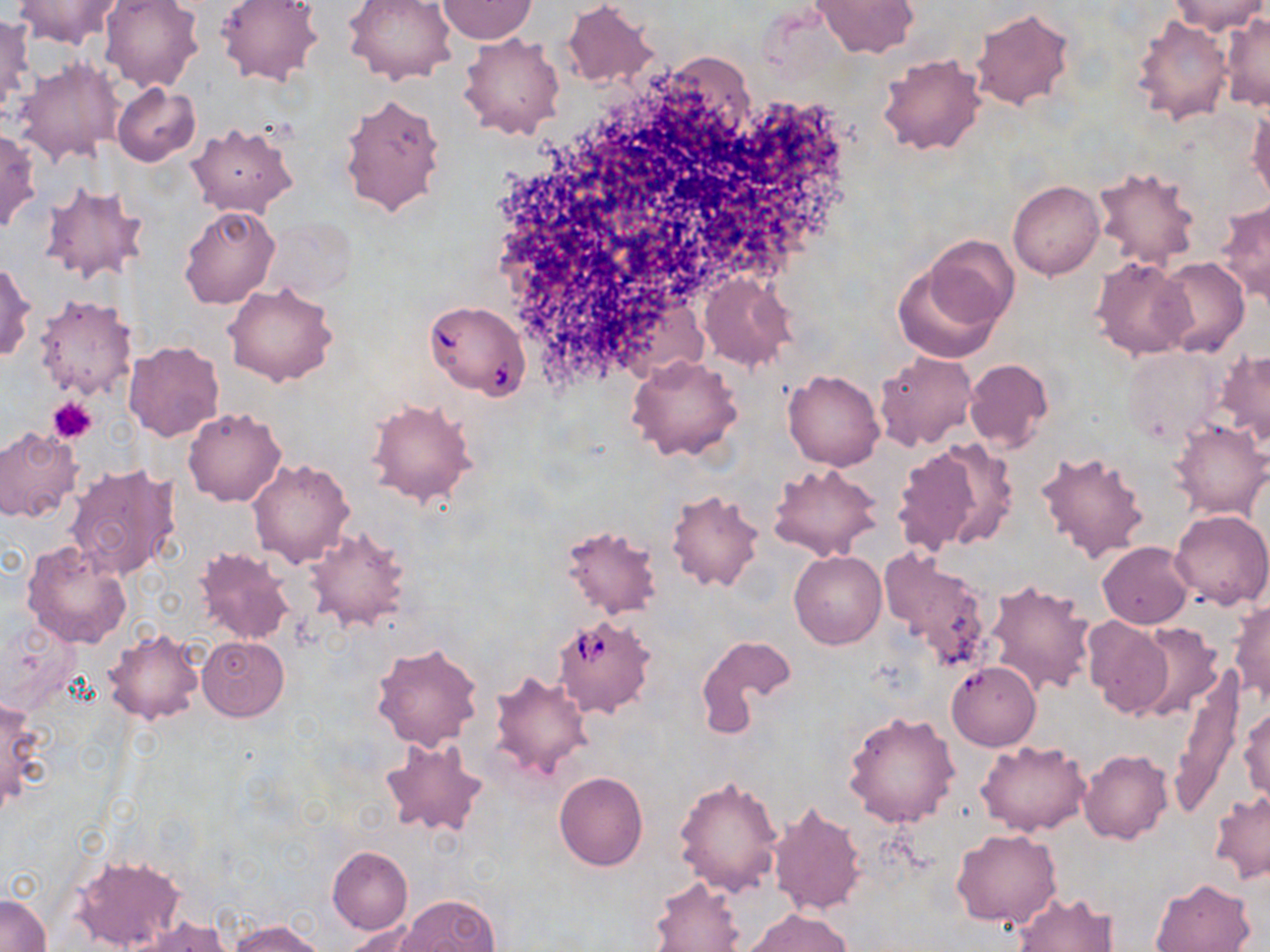

{
  "slide_level_diagnosis": "Babesia divergens",
  "stain": "May-Grünwald-Giemsa",
  "modality": "light microscopy",
  "magnification": "1000x",
  "babesia_divergens_infected_red_blood_cell_locations": "approximate bounding boxes as named x1/y1/x2/y2 corners in pixels: (x1=424, y1=300, x2=529, y2=400), (x1=552, y1=613, x2=658, y2=720)",
  "field_of_view": "one of a larger specimen",
  "uninfected_red_blood_cell_locations": "approximate bounding boxes as named x1/y1/x2/y2 corners in pixels: (x1=10, y1=0, x2=126, y2=49), (x1=100, y1=0, x2=204, y2=92), (x1=216, y1=0, x2=323, y2=87), (x1=343, y1=0, x2=457, y2=85), (x1=811, y1=0, x2=919, y2=57), (x1=1169, y1=0, x2=1265, y2=36), (x1=437, y1=1, x2=537, y2=44), (x1=561, y1=2, x2=659, y2=89), (x1=970, y1=7, x2=1075, y2=111), (x1=0, y1=14, x2=32, y2=122), (x1=1220, y1=14, x2=1270, y2=110), (x1=1133, y1=16, x2=1231, y2=124), (x1=459, y1=32, x2=565, y2=140), (x1=877, y1=51, x2=984, y2=155), (x1=13, y1=56, x2=123, y2=167), (x1=112, y1=82, x2=201, y2=167), (x1=338, y1=91, x2=446, y2=218), (x1=1248, y1=104, x2=1269, y2=205), (x1=187, y1=121, x2=298, y2=217), (x1=0, y1=129, x2=40, y2=234), (x1=1092, y1=165, x2=1202, y2=268), (x1=1007, y1=179, x2=1104, y2=280), (x1=39, y1=181, x2=150, y2=286), (x1=1215, y1=199, x2=1270, y2=305), (x1=178, y1=204, x2=280, y2=310), (x1=264, y1=218, x2=355, y2=301), (x1=924, y1=235, x2=1019, y2=332), (x1=1090, y1=257, x2=1194, y2=360), (x1=1155, y1=258, x2=1249, y2=358), (x1=0, y1=259, x2=35, y2=363), (x1=891, y1=260, x2=1005, y2=365), (x1=700, y1=273, x2=796, y2=372), (x1=222, y1=281, x2=338, y2=388), (x1=33, y1=295, x2=138, y2=401), (x1=122, y1=340, x2=225, y2=442), (x1=1121, y1=348, x2=1224, y2=445), (x1=1216, y1=350, x2=1270, y2=446), (x1=876, y1=351, x2=977, y2=450), (x1=628, y1=354, x2=743, y2=461), (x1=964, y1=357, x2=1053, y2=453), (x1=783, y1=369, x2=885, y2=471), (x1=367, y1=396, x2=477, y2=508), (x1=182, y1=406, x2=286, y2=506), (x1=1168, y1=420, x2=1269, y2=520), (x1=0, y1=427, x2=82, y2=522), (x1=893, y1=440, x2=1010, y2=555), (x1=1035, y1=449, x2=1150, y2=563), (x1=248, y1=457, x2=355, y2=568), (x1=63, y1=462, x2=181, y2=580), (x1=768, y1=462, x2=885, y2=563), (x1=666, y1=488, x2=764, y2=592), (x1=1168, y1=509, x2=1269, y2=610), (x1=305, y1=525, x2=410, y2=632), (x1=560, y1=525, x2=663, y2=621), (x1=1098, y1=540, x2=1194, y2=628), (x1=22, y1=541, x2=133, y2=648), (x1=192, y1=546, x2=295, y2=646), (x1=880, y1=548, x2=993, y2=672), (x1=789, y1=550, x2=886, y2=648), (x1=984, y1=579, x2=1096, y2=698), (x1=1229, y1=602, x2=1270, y2=703), (x1=1082, y1=616, x2=1173, y2=717), (x1=1129, y1=622, x2=1225, y2=720), (x1=104, y1=628, x2=204, y2=725), (x1=197, y1=635, x2=288, y2=721), (x1=697, y1=635, x2=796, y2=736), (x1=371, y1=643, x2=482, y2=750), (x1=944, y1=662, x2=1041, y2=751), (x1=1174, y1=662, x2=1244, y2=812), (x1=487, y1=670, x2=593, y2=785), (x1=0, y1=702, x2=49, y2=806), (x1=1240, y1=706, x2=1270, y2=799), (x1=843, y1=710, x2=960, y2=828), (x1=380, y1=737, x2=490, y2=838), (x1=977, y1=739, x2=1091, y2=837), (x1=1078, y1=749, x2=1173, y2=844), (x1=554, y1=772, x2=647, y2=870), (x1=673, y1=773, x2=783, y2=897), (x1=1208, y1=790, x2=1270, y2=885), (x1=767, y1=800, x2=868, y2=918), (x1=952, y1=829, x2=1062, y2=928), (x1=327, y1=845, x2=412, y2=934), (x1=69, y1=853, x2=186, y2=952), (x1=648, y1=875, x2=745, y2=951), (x1=1150, y1=878, x2=1255, y2=952), (x1=1013, y1=892, x2=1119, y2=952), (x1=1, y1=893, x2=51, y2=951), (x1=397, y1=894, x2=501, y2=952), (x1=744, y1=909, x2=853, y2=952), (x1=125, y1=917, x2=231, y2=952), (x1=230, y1=919, x2=327, y2=952), (x1=347, y1=922, x2=432, y2=951)",
  "preparation": "thin blood film",
  "image_size": "1270×952 pixels",
  "platelet_locations": "approximate bounding boxes as named x1/y1/x2/y2 corners in pixels: (x1=49, y1=397, x2=97, y2=443)"
}